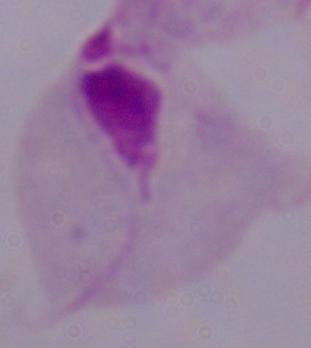
Summary:
  - Identification: trichomonad
  - Magnification: 1000x
  - Modality: micrograph